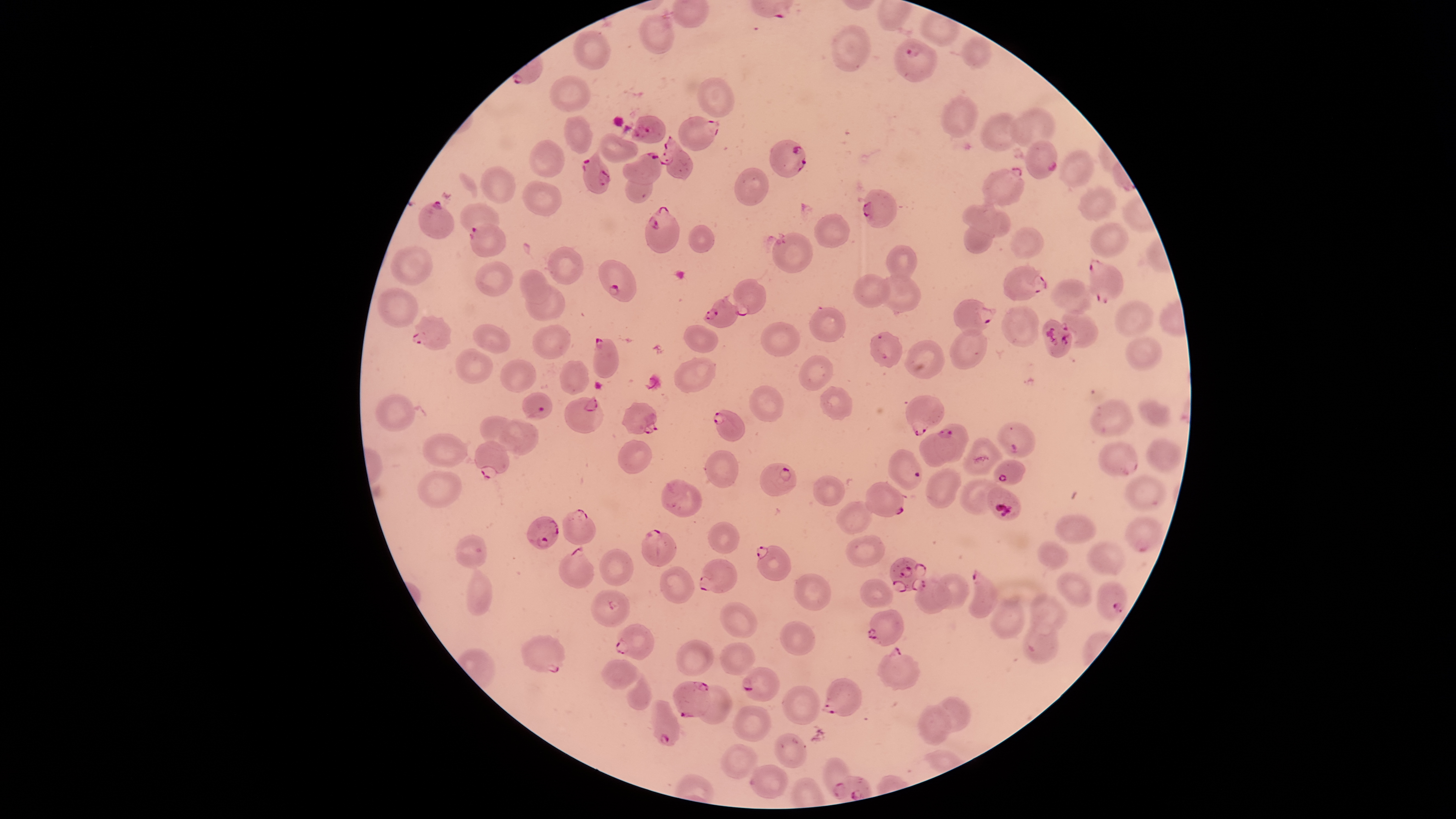
species = Plasmodium falciparum
capture = smartphone photograph through the microscope eyepiece
parasitized RBCs = approximate bounding boxes as [left, top, right, bottom] in pixels: [895, 38, 939, 82], [632, 115, 665, 143], [679, 117, 720, 151], [659, 135, 692, 180], [769, 140, 807, 177], [1024, 140, 1057, 179], [581, 147, 609, 194], [622, 152, 661, 186], [980, 166, 1024, 206], [862, 189, 896, 229], [417, 200, 454, 238], [646, 205, 681, 254], [468, 223, 506, 257], [1089, 256, 1123, 305], [597, 260, 637, 303], [1003, 262, 1048, 300], [731, 279, 766, 317], [703, 297, 739, 328], [953, 297, 996, 336], [411, 316, 451, 350], [594, 338, 620, 378], [523, 392, 553, 421], [904, 395, 943, 435], [564, 396, 604, 432], [622, 402, 658, 435], [712, 410, 743, 441], [997, 421, 1034, 459], [919, 423, 968, 468], [476, 439, 510, 479], [1099, 441, 1137, 475], [993, 459, 1026, 486], [760, 463, 796, 496], [866, 482, 904, 517], [561, 509, 596, 545], [526, 515, 560, 550], [1125, 518, 1164, 554], [640, 529, 677, 568], [559, 545, 595, 590], [756, 545, 790, 580], [699, 558, 736, 594], [888, 558, 926, 594], [969, 568, 997, 618], [1097, 580, 1129, 620], [867, 608, 904, 645], [614, 624, 655, 661], [521, 635, 565, 673], [880, 645, 921, 691], [741, 667, 778, 702], [821, 678, 862, 715], [672, 681, 712, 718], [652, 700, 679, 746], [823, 758, 851, 799]
field of view = single
preparation = thin smear of blood
stain = Giemsa
uninfected RBCs = approximate bounding boxes as [left, top, right, bottom] in pixels: [638, 14, 675, 54], [831, 26, 872, 72], [573, 30, 610, 68], [959, 36, 992, 68], [549, 76, 590, 112], [697, 78, 734, 117], [941, 96, 977, 138], [1010, 109, 1055, 149], [981, 112, 1024, 149], [563, 115, 594, 154], [599, 134, 639, 164], [529, 139, 565, 177], [1059, 149, 1094, 186], [626, 165, 654, 203], [480, 167, 515, 204], [735, 168, 769, 206], [521, 180, 563, 216], [1078, 187, 1115, 222], [963, 198, 997, 254], [460, 202, 500, 239], [963, 204, 1012, 238], [815, 214, 849, 246], [1091, 222, 1128, 258], [689, 224, 715, 254], [1012, 228, 1044, 258], [772, 232, 813, 274], [886, 244, 918, 281], [389, 247, 433, 285], [549, 248, 584, 285], [474, 262, 512, 297], [519, 268, 549, 305], [853, 274, 890, 307], [874, 275, 920, 311], [1052, 280, 1093, 315], [525, 284, 565, 321], [377, 287, 419, 328], [1114, 300, 1156, 337], [1002, 305, 1038, 347], [808, 307, 845, 341], [1061, 309, 1097, 347], [761, 323, 799, 357], [473, 324, 510, 353], [532, 325, 572, 359], [685, 325, 717, 352], [949, 328, 987, 370], [870, 331, 903, 368], [1125, 337, 1162, 370], [904, 340, 945, 380], [456, 348, 494, 385], [673, 357, 715, 394], [798, 357, 831, 392], [500, 359, 535, 392], [559, 361, 588, 395], [748, 386, 784, 422], [819, 386, 852, 421], [376, 393, 415, 430], [1091, 398, 1134, 437], [1139, 398, 1172, 427], [480, 415, 529, 451], [500, 421, 538, 456], [423, 433, 468, 468], [963, 435, 1003, 476], [1145, 439, 1182, 473], [618, 441, 652, 473], [706, 451, 738, 488], [926, 468, 961, 510], [417, 470, 463, 507], [1125, 473, 1166, 512], [813, 475, 845, 506], [959, 478, 1003, 514], [662, 481, 702, 518], [837, 500, 874, 534], [1054, 514, 1098, 542], [709, 521, 739, 553], [455, 535, 486, 568], [845, 535, 884, 567], [1038, 542, 1068, 569], [1087, 542, 1125, 575], [599, 548, 633, 586], [659, 566, 696, 604], [465, 567, 492, 615], [794, 572, 832, 610], [932, 572, 969, 610], [1056, 572, 1093, 608], [915, 577, 951, 615], [860, 578, 894, 608], [591, 590, 630, 628], [1030, 594, 1067, 635], [989, 596, 1024, 638], [719, 602, 758, 638], [1024, 620, 1058, 663], [780, 621, 817, 655], [676, 639, 715, 677], [719, 643, 756, 675], [602, 659, 638, 690], [626, 673, 652, 709], [695, 685, 732, 724], [782, 685, 821, 724], [932, 697, 971, 732], [919, 703, 951, 746], [732, 704, 772, 742], [774, 734, 807, 768], [721, 745, 758, 778], [750, 764, 788, 798]
presence = malaria parasites seen
image size = 1456×819 pixels
visible region = circular